Give the position of every Plasmodium parasite visible.
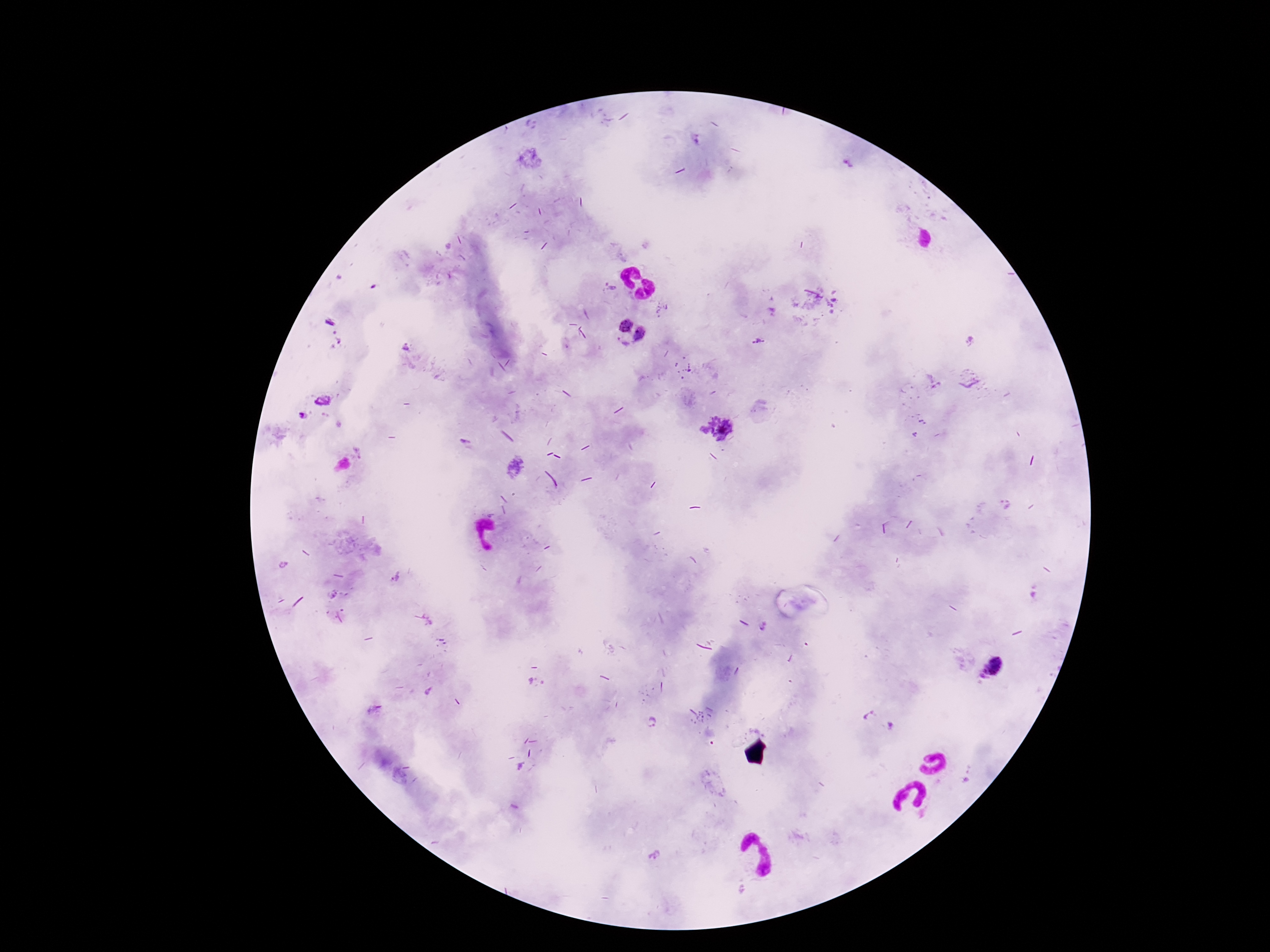
Approximate centers as [x, y] in pixels.
Plasmodium parasites: [625, 325], [639, 335], [758, 341], [405, 345], [621, 345], [323, 401], [305, 416], [723, 427], [703, 430], [465, 441], [359, 452], [516, 467], [763, 629], [993, 668], [870, 717], [651, 722], [890, 725], [655, 855].

preparation = thick blood film
capture = smartphone camera through the microscope eyepiece
image size = 1270×952 pixels
stain = Giemsa
patient malaria status = positive
magnification = 100x
field of view = one from this slide